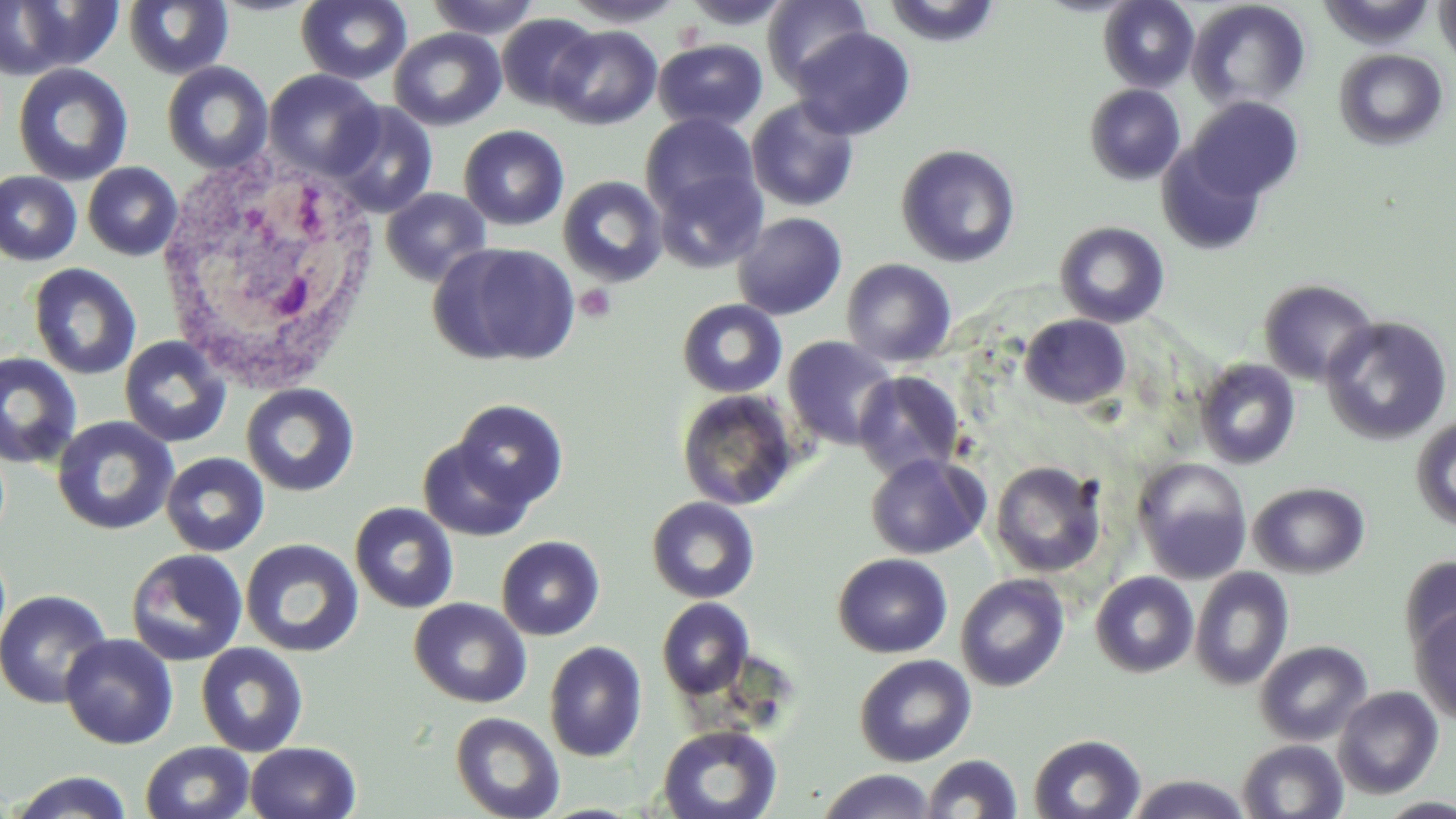
Summary:
  - Coordinate format: approximate bounding boxes as named x1/y1/x2/y2 corners in pixels
  - Uninfected red blood cell locations: (x1=0, y1=0, x2=123, y2=81), (x1=426, y1=0, x2=542, y2=39), (x1=563, y1=0, x2=687, y2=27), (x1=681, y1=0, x2=795, y2=30), (x1=763, y1=0, x2=872, y2=88), (x1=881, y1=0, x2=1002, y2=47), (x1=1099, y1=0, x2=1198, y2=91), (x1=1187, y1=0, x2=1312, y2=111), (x1=1435, y1=0, x2=1456, y2=69), (x1=123, y1=1, x2=234, y2=80), (x1=295, y1=1, x2=412, y2=85), (x1=496, y1=14, x2=600, y2=111), (x1=547, y1=25, x2=662, y2=130), (x1=389, y1=27, x2=506, y2=131), (x1=790, y1=27, x2=916, y2=140), (x1=653, y1=38, x2=768, y2=132), (x1=1334, y1=49, x2=1449, y2=150), (x1=161, y1=61, x2=274, y2=173), (x1=13, y1=62, x2=133, y2=186), (x1=264, y1=70, x2=383, y2=179), (x1=1084, y1=84, x2=1185, y2=185), (x1=1187, y1=96, x2=1304, y2=201), (x1=746, y1=97, x2=859, y2=212), (x1=328, y1=102, x2=439, y2=218), (x1=640, y1=112, x2=761, y2=220), (x1=459, y1=125, x2=569, y2=230), (x1=1157, y1=142, x2=1268, y2=255), (x1=896, y1=144, x2=1021, y2=267), (x1=83, y1=162, x2=183, y2=260), (x1=654, y1=168, x2=766, y2=274), (x1=0, y1=171, x2=81, y2=266), (x1=557, y1=176, x2=668, y2=286), (x1=381, y1=188, x2=492, y2=286), (x1=733, y1=212, x2=847, y2=320), (x1=1054, y1=221, x2=1170, y2=328), (x1=430, y1=242, x2=581, y2=367), (x1=841, y1=258, x2=956, y2=367), (x1=28, y1=263, x2=141, y2=380), (x1=1259, y1=279, x2=1378, y2=385), (x1=677, y1=299, x2=788, y2=398), (x1=1019, y1=314, x2=1131, y2=409), (x1=1320, y1=315, x2=1453, y2=446), (x1=782, y1=335, x2=898, y2=450), (x1=119, y1=336, x2=232, y2=448), (x1=0, y1=353, x2=83, y2=469), (x1=1194, y1=358, x2=1301, y2=469), (x1=853, y1=370, x2=965, y2=481), (x1=241, y1=383, x2=359, y2=497), (x1=676, y1=389, x2=800, y2=511), (x1=451, y1=399, x2=568, y2=510), (x1=1411, y1=415, x2=1456, y2=531), (x1=52, y1=416, x2=179, y2=536), (x1=418, y1=436, x2=536, y2=541), (x1=161, y1=452, x2=269, y2=556), (x1=865, y1=453, x2=989, y2=559), (x1=1132, y1=458, x2=1252, y2=581), (x1=990, y1=460, x2=1107, y2=577), (x1=1248, y1=481, x2=1370, y2=579), (x1=646, y1=496, x2=760, y2=603), (x1=349, y1=502, x2=459, y2=614), (x1=495, y1=535, x2=605, y2=640), (x1=240, y1=538, x2=364, y2=658), (x1=125, y1=549, x2=248, y2=666), (x1=832, y1=553, x2=953, y2=658), (x1=1399, y1=555, x2=1456, y2=660), (x1=1190, y1=567, x2=1294, y2=690), (x1=1090, y1=571, x2=1199, y2=677), (x1=956, y1=574, x2=1069, y2=691), (x1=0, y1=589, x2=113, y2=709), (x1=409, y1=598, x2=531, y2=708), (x1=657, y1=598, x2=754, y2=698), (x1=1410, y1=607, x2=1456, y2=724), (x1=60, y1=634, x2=179, y2=749), (x1=544, y1=640, x2=648, y2=763), (x1=1255, y1=640, x2=1372, y2=746), (x1=195, y1=642, x2=308, y2=757), (x1=854, y1=654, x2=976, y2=767), (x1=1333, y1=686, x2=1444, y2=799), (x1=450, y1=711, x2=565, y2=819), (x1=657, y1=724, x2=783, y2=819), (x1=1028, y1=733, x2=1147, y2=818), (x1=1237, y1=739, x2=1349, y2=818), (x1=140, y1=741, x2=256, y2=819), (x1=246, y1=741, x2=361, y2=819), (x1=922, y1=753, x2=1022, y2=818), (x1=817, y1=769, x2=940, y2=819), (x1=7, y1=771, x2=135, y2=819), (x1=1125, y1=774, x2=1253, y2=818), (x1=1375, y1=797, x2=1456, y2=818), (x1=537, y1=803, x2=647, y2=819)
  - Platelet locations: (x1=576, y1=283, x2=618, y2=324)
  - White blood cell locations: (x1=154, y1=154, x2=387, y2=392)
  - Slide-level diagnosis: negative for blood parasites
  - Field of view: one of a larger specimen
  - Magnification: 1000x
  - Modality: optical microscopy
  - Stain: May-Grünwald-Giemsa
  - Preparation: thin blood smear
  - Image size: 1456×819 pixels